Give the extent of all Plasmodium falciparum-infected red blood cells.
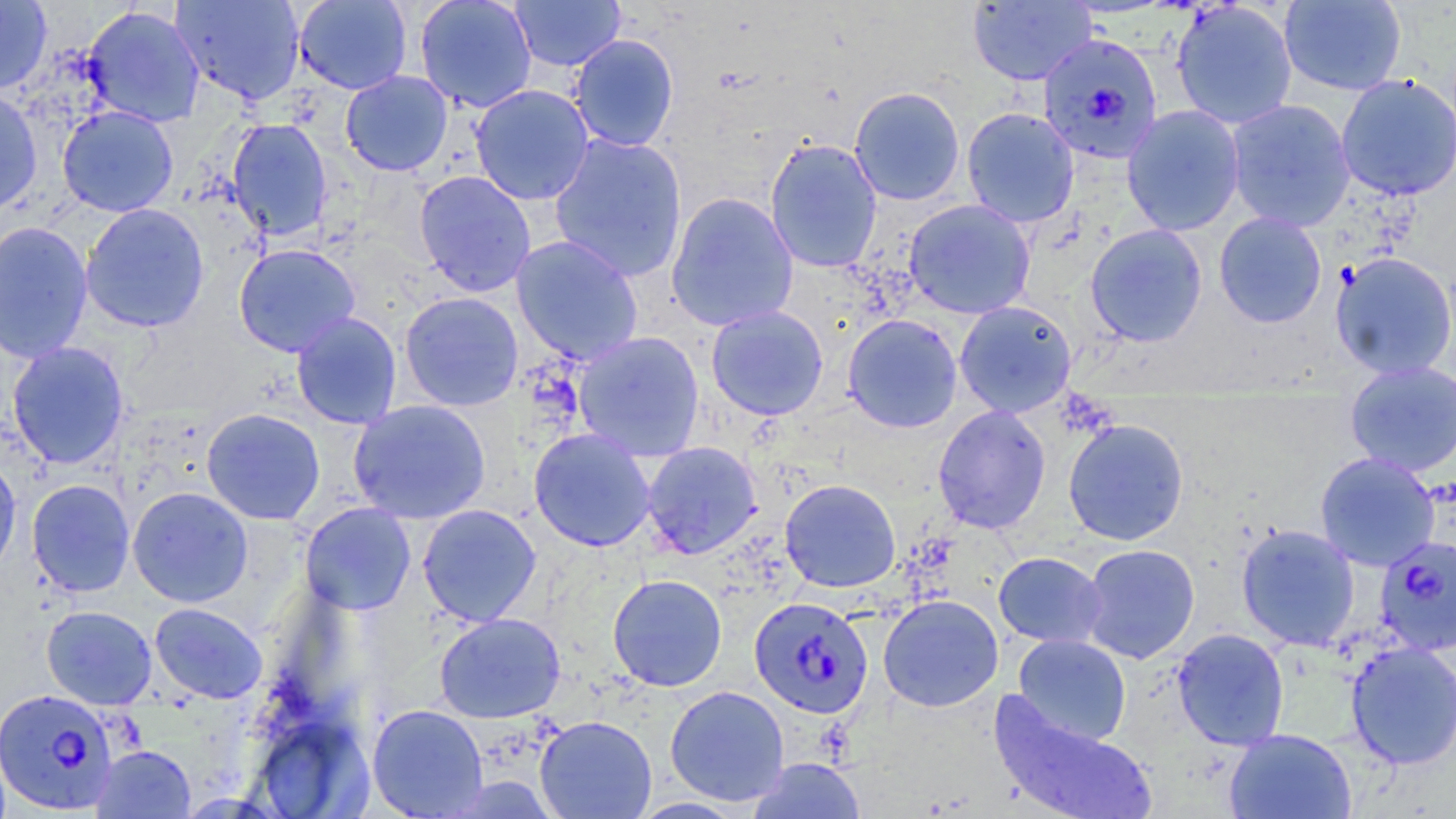
Approximate bounding boxes as [x1, y1, x2, y2] in pixels.
Plasmodium falciparum-infected red blood cells: [1038, 32, 1163, 164], [1373, 534, 1456, 657], [748, 597, 874, 718], [0, 687, 119, 815].

Uninfected red blood cell locations: [170, 0, 306, 105], [294, 0, 412, 95], [414, 0, 537, 113], [509, 0, 625, 72], [966, 0, 1096, 86], [1277, 0, 1407, 96], [0, 1, 52, 93], [1171, 2, 1298, 130], [81, 6, 205, 127], [569, 33, 680, 152], [340, 70, 453, 177], [1335, 74, 1456, 201], [470, 85, 595, 205], [849, 86, 965, 206], [0, 87, 42, 214], [1225, 99, 1355, 232], [1121, 104, 1245, 236], [57, 105, 179, 217], [961, 107, 1080, 227], [225, 118, 333, 241], [548, 133, 688, 282], [765, 138, 882, 274], [413, 170, 537, 297], [665, 192, 799, 332], [903, 199, 1036, 319], [80, 203, 210, 332], [1214, 212, 1327, 328], [0, 220, 93, 364], [1085, 224, 1207, 346], [511, 235, 644, 366], [233, 243, 361, 357], [1330, 252, 1456, 380], [399, 291, 524, 411], [954, 300, 1077, 418], [706, 305, 829, 420], [290, 311, 402, 430], [842, 314, 962, 433], [572, 331, 705, 461], [6, 341, 129, 470], [1343, 360, 1456, 476], [348, 399, 492, 524], [932, 405, 1051, 534], [201, 408, 325, 524], [1062, 418, 1189, 546], [528, 428, 656, 552], [641, 441, 762, 559], [1315, 452, 1440, 571], [0, 455, 21, 579], [26, 479, 135, 597], [780, 479, 901, 592], [127, 487, 253, 607], [300, 502, 416, 615], [417, 504, 542, 626], [1236, 523, 1360, 651], [1080, 543, 1200, 663], [993, 551, 1107, 648], [608, 574, 727, 692], [878, 594, 1003, 712], [149, 602, 268, 704], [41, 605, 157, 709], [434, 612, 566, 723], [1172, 628, 1289, 751], [1013, 634, 1131, 745], [1345, 641, 1456, 769], [664, 685, 789, 806], [988, 694, 1156, 819], [367, 703, 488, 818], [535, 715, 657, 819], [256, 718, 372, 818], [1223, 728, 1357, 819], [91, 745, 195, 818], [749, 759, 866, 818]. Slide-level diagnosis: Plasmodium falciparum. May-Grünwald-Giemsa stain. Light microscopy. 1000x magnification. Thin blood film. Image is 1456×819 pixels. Single field of view.